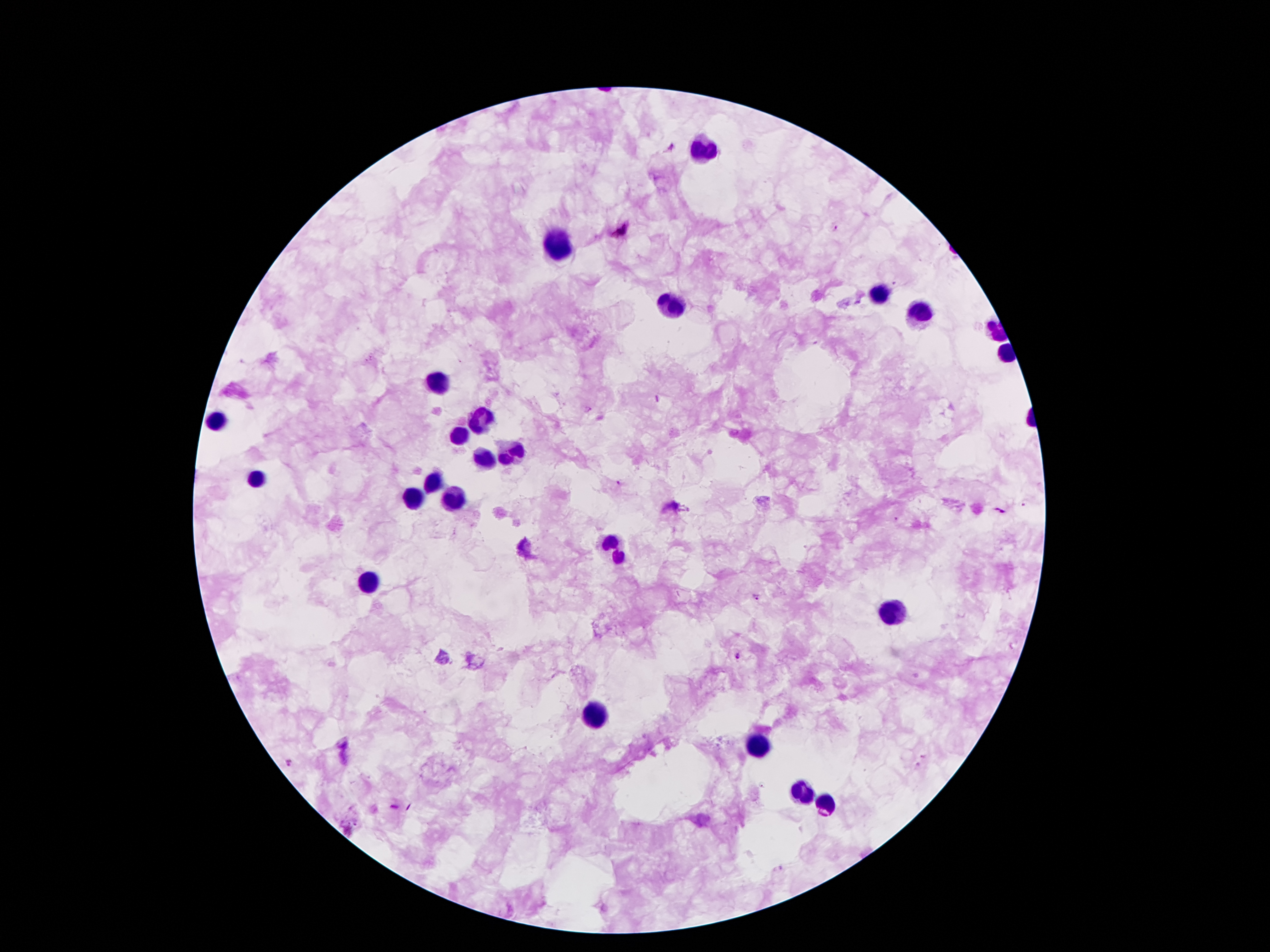

Approximate object centers, in pixels from the top-left corner. Plasmodium parasite locations: (x=836, y=228), (x=622, y=229), (x=617, y=481), (x=1025, y=503), (x=1000, y=510), (x=755, y=597), (x=739, y=655), (x=923, y=756), (x=290, y=763). Leukocyte locations: (x=705, y=147), (x=550, y=246), (x=881, y=294), (x=675, y=305), (x=923, y=313), (x=436, y=382), (x=480, y=420), (x=214, y=422), (x=457, y=435), (x=510, y=450), (x=484, y=462), (x=255, y=479), (x=434, y=485), (x=413, y=498), (x=455, y=500), (x=615, y=546), (x=369, y=580), (x=890, y=614), (x=592, y=717), (x=757, y=746), (x=802, y=790), (x=825, y=805). 100x magnification. Patient malaria status: infected with Plasmodium falciparum. Image is 1270×952 pixels. Giemsa-stained preparation. One field from this slide. Thick blood smear. Smartphone photograph taken through the microscope eyepiece.